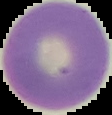
{
  "image_size": "112×115 pixels",
  "image_type": "segmented cell region with the area outside set to black",
  "result": "no malaria parasites seen",
  "preparation": "thin blood smear"
}